Locate platelets.
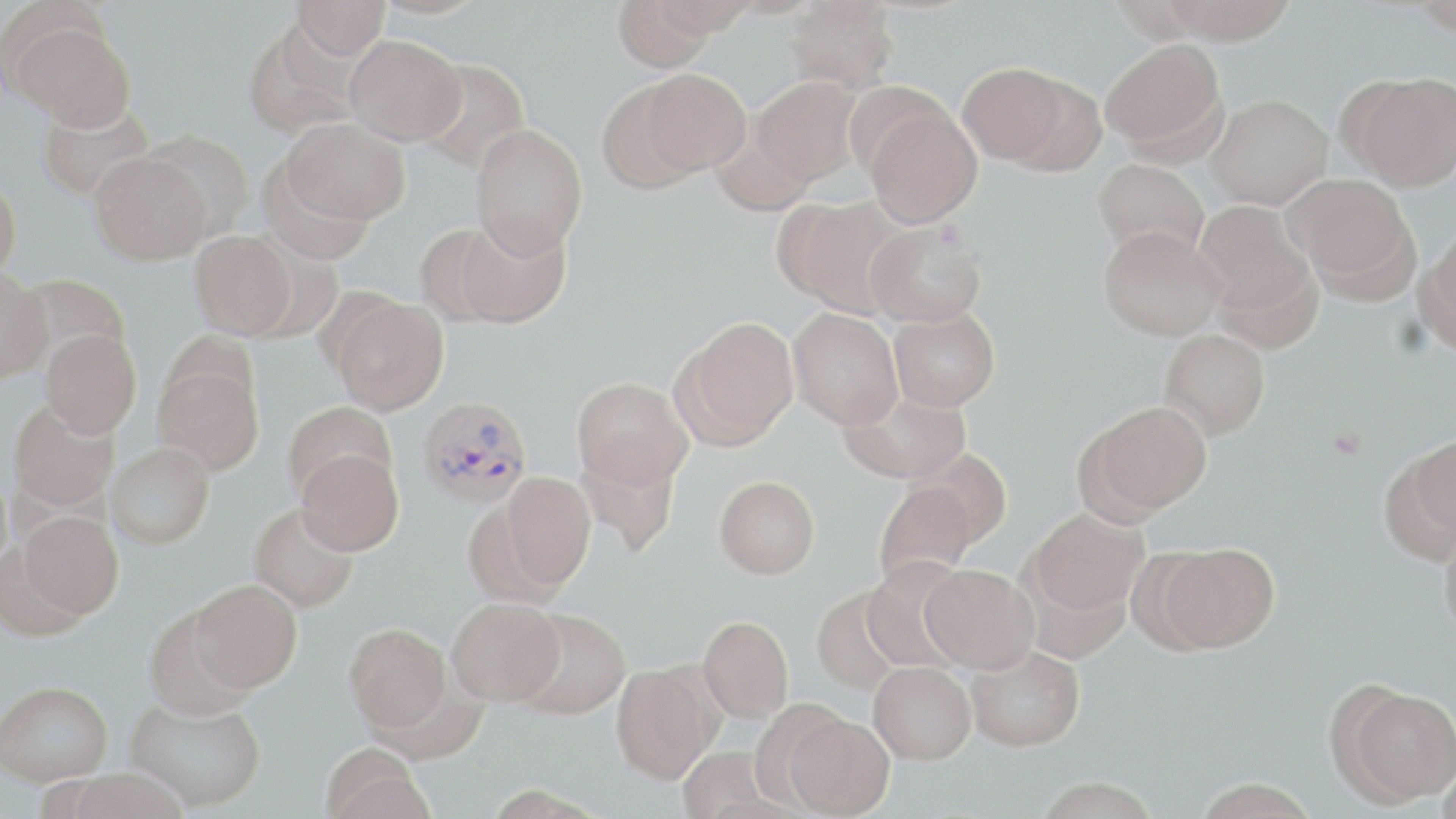

Approximate bounding boxes as (x1,y1)-(x2,y2) corner pairs in pixels.
Platelets: (1326,425)-(1369,459).

Plasmodium vivax-infected red blood cell locations: (418,395)-(533,509). Uninfected red blood cell locations: (293,0)-(390,60), (611,0)-(722,72), (785,0)-(900,93), (1161,0)-(1299,44), (1412,1)-(1455,35), (9,18)-(135,131), (241,20)-(361,138), (344,33)-(467,145), (1099,38)-(1226,156), (415,59)-(531,174), (958,62)-(1069,165), (638,68)-(751,176), (1349,73)-(1456,191), (751,76)-(864,186), (1003,76)-(1107,178), (596,80)-(703,194), (1207,94)-(1332,209), (35,101)-(155,204), (862,101)-(982,228), (283,118)-(410,226), (471,123)-(588,259), (709,127)-(814,218), (143,130)-(255,241), (89,150)-(212,265), (1094,159)-(1209,262), (0,174)-(22,282), (1286,174)-(1415,293), (777,196)-(908,316), (1194,200)-(1316,325), (448,215)-(572,328), (865,222)-(986,327), (414,223)-(514,325), (1098,225)-(1225,341), (190,230)-(298,340), (1421,230)-(1456,352), (0,268)-(51,382), (21,273)-(132,366), (329,296)-(449,415), (888,307)-(1000,411), (788,309)-(903,429), (676,317)-(799,448), (40,329)-(141,438), (1158,329)-(1270,440), (153,360)-(265,476), (572,377)-(692,489), (840,388)-(970,485), (8,399)-(119,514), (282,401)-(398,500), (1082,401)-(1212,518), (1412,430)-(1456,548), (105,442)-(214,549), (575,445)-(682,557), (296,449)-(404,556), (908,449)-(1011,548), (500,472)-(596,592), (715,475)-(819,579), (873,481)-(978,587), (249,502)-(358,613), (1026,508)-(1148,617), (18,511)-(123,619), (1440,523)-(1456,646), (1157,543)-(1279,653), (861,559)-(970,672), (921,564)-(1039,674), (189,579)-(302,693), (812,588)-(906,695), (447,598)-(564,705), (143,604)-(257,719), (511,607)-(631,720), (699,615)-(793,722), (345,622)-(452,734), (965,644)-(1085,752), (869,660)-(976,764), (611,663)-(718,784), (1,680)-(113,785), (1336,684)-(1456,806), (125,694)-(266,812), (783,713)-(895,818), (319,744)-(434,819), (676,746)-(778,818), (1436,762)-(1456,819), (1033,777)-(1163,819), (1192,778)-(1321,819). Slide-level diagnosis: Plasmodium vivax. Thin blood film. May-Grünwald-Giemsa-stained preparation. Optical microscopy. Single field of view. 1000x magnification. Image is 1456×819 pixels.